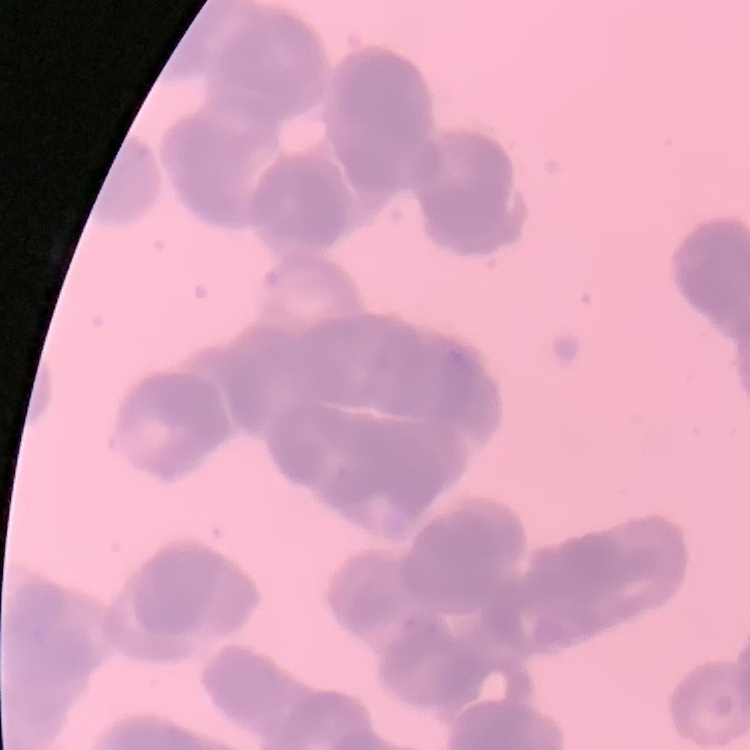

Summary:
  - Red blood cell morphology: rouleaux formation
  - Stain: Field's or Giemsa
  - Image type: square crop of a larger photomicrograph
  - Preparation: thin peripheral smear